Name the parasite shown.
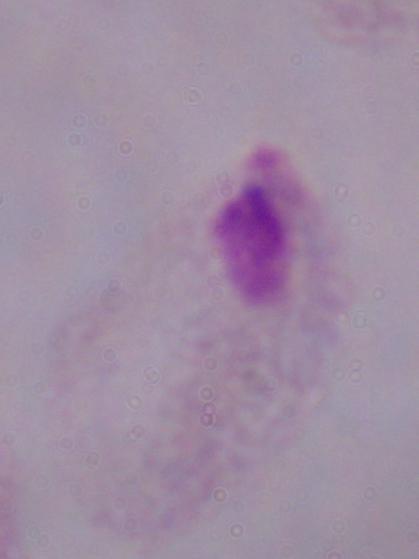

This is a trichomonad.

{
  "modality": "micrograph",
  "magnification": "1000x"
}